Name the parasite shown.
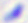
This is Toxoplasma gondii.

Captured at 400x magnification. Photomicrograph.